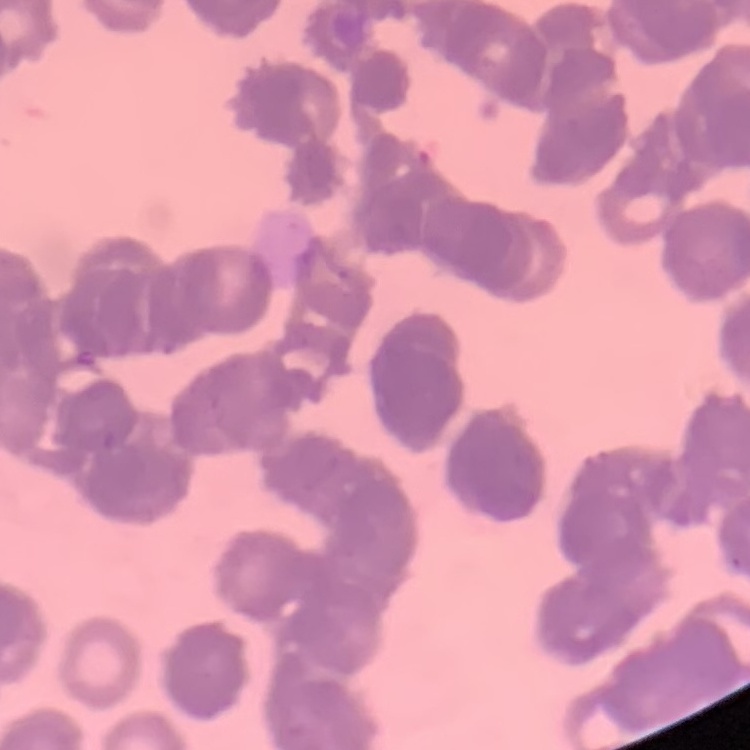

Summary:
  - Erythrocyte morphology: rouleaux formation
  - Preparation: thin peripheral smear
  - Image type: one tile cut from a larger photomicrograph
  - Stain: Field's or Giemsa